State which parasite is depicted.
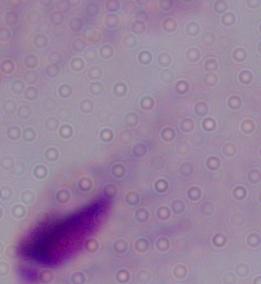

This is a trichomonad.

{
  "magnification": "1000x",
  "modality": "photomicrograph"
}